Give the position of every Plasmodium parasite.
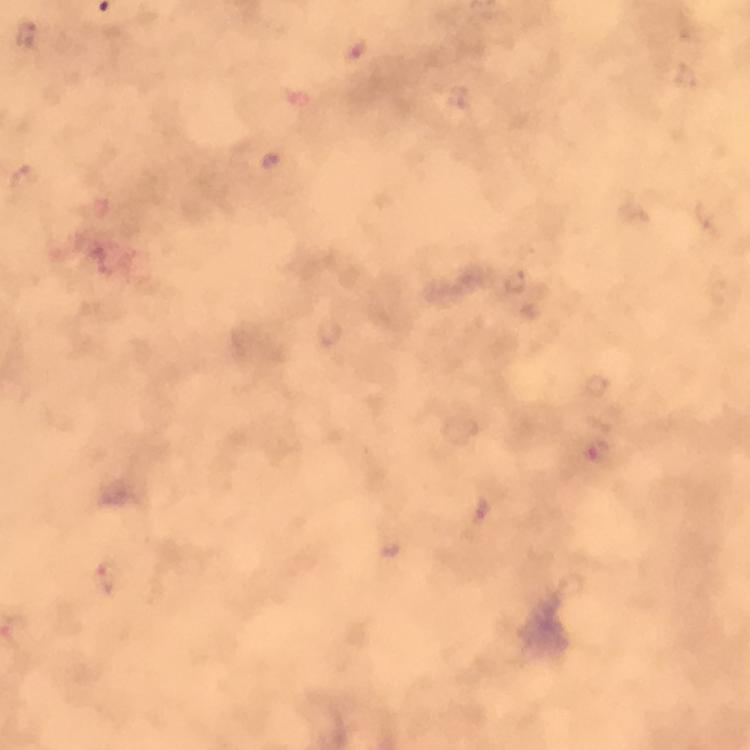

Approximate object centers, in pixels from the top-left corner.
Plasmodium parasites: (x=26, y=34), (x=272, y=158), (x=517, y=281), (x=593, y=453), (x=483, y=511), (x=108, y=578).

Smartphone photograph taken through a microscope. Image is 750×750 pixels. Thick blood smear. Cropped region of a single field of view. Giemsa stain. From a malaria diagnostic workup. Immersion oil applied. 100x magnification.